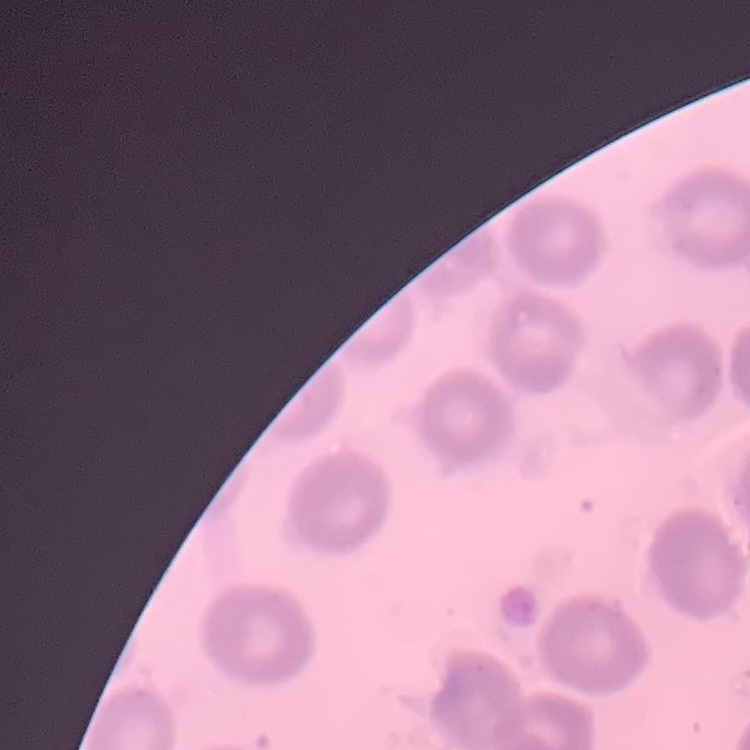
Summary:
  - Erythrocyte morphology: no rouleaux formation
  - Image type: square crop of a larger photomicrograph
  - Preparation: thin blood film
  - Stain: Field's or Giemsa